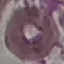

Summary:
  - Malaria status: uninfected
  - Capture: smartphone through the microscope eyepiece
  - Image type: cell patch, automatically extracted from a larger field of view and resized to 64 × 64 pixels
  - Preparation: thin smear
  - Stain: Giemsa